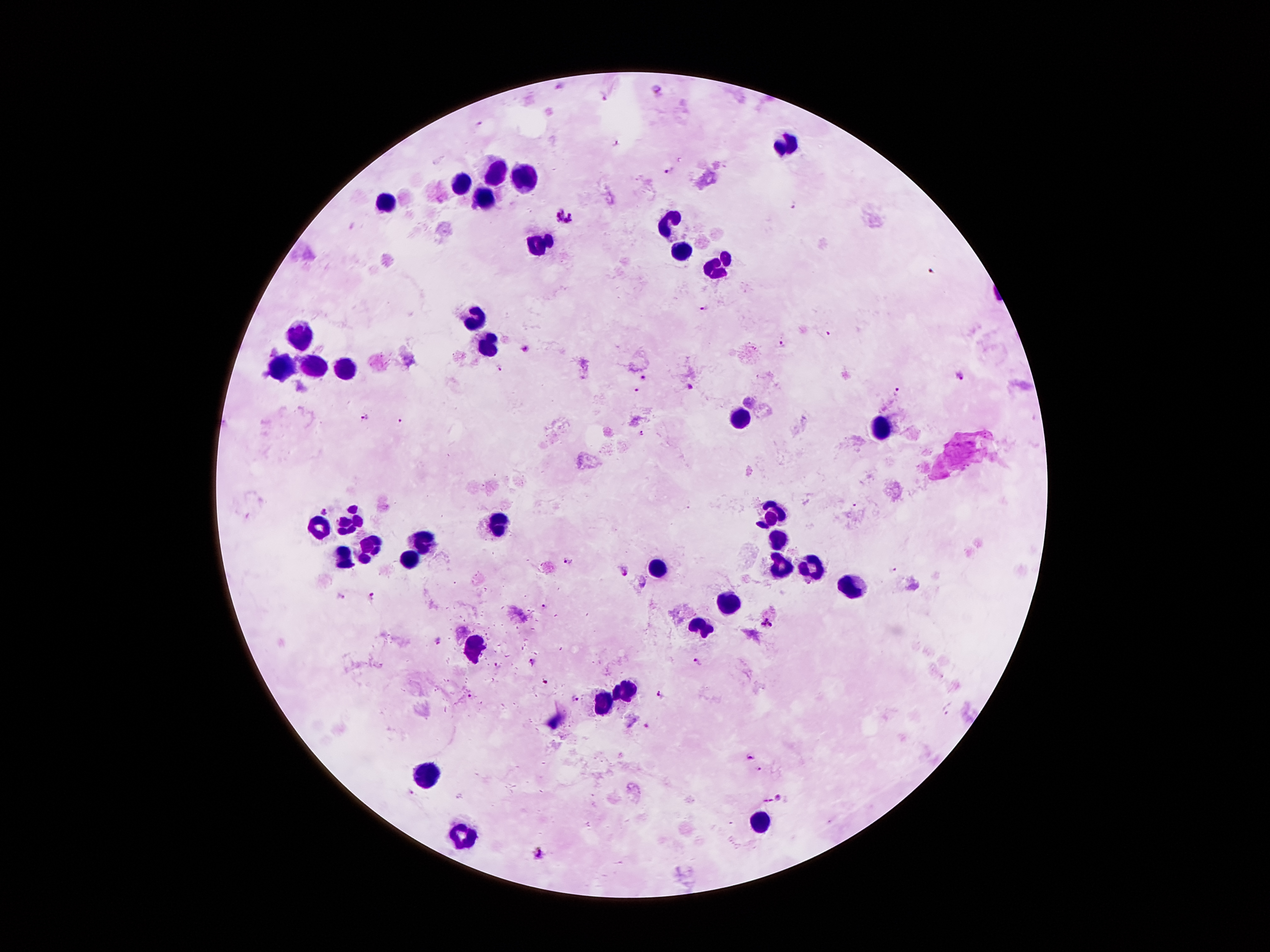
coordinate format = approximate centers as {x, y} in pixels
leukocyte locations = {786, 146}, {494, 169}, {528, 182}, {464, 185}, {484, 199}, {387, 201}, {670, 223}, {537, 244}, {682, 249}, {718, 266}, {473, 317}, {296, 339}, {487, 339}, {280, 362}, {312, 366}, {344, 371}, {739, 417}, {881, 428}, {770, 516}, {353, 521}, {494, 523}, {318, 525}, {779, 539}, {423, 541}, {369, 548}, {343, 560}, {405, 562}, {805, 564}, {659, 566}, {779, 566}, {850, 585}, {730, 600}, {702, 626}, {473, 646}, {625, 691}, {602, 701}, {423, 780}, {755, 825}, {462, 832}
malaria parasite locations = {561, 85}, {655, 88}, {605, 96}, {479, 124}, {617, 142}, {668, 169}, {794, 204}, {565, 218}, {931, 270}, {704, 308}, {827, 333}, {783, 345}, {526, 348}, {499, 366}, {961, 376}, {643, 378}, {690, 386}, {635, 388}, {897, 390}, {365, 416}, {401, 421}, {641, 433}, {857, 504}, {323, 509}, {569, 562}, {892, 570}, {625, 574}, {642, 585}, {341, 596}, {372, 596}, {545, 608}, {766, 624}, {436, 641}, {699, 661}, {531, 663}, {497, 666}, {545, 679}, {662, 694}, {471, 697}, {574, 699}, {647, 725}, {750, 756}, {779, 798}, {536, 853}
image size = 1270×952 pixels
stain = Giemsa
field of view = one from this slide
magnification = 100x
preparation = thick blood film
patient malaria status = infected with Plasmodium falciparum
capture = smartphone camera through the microscope eyepiece